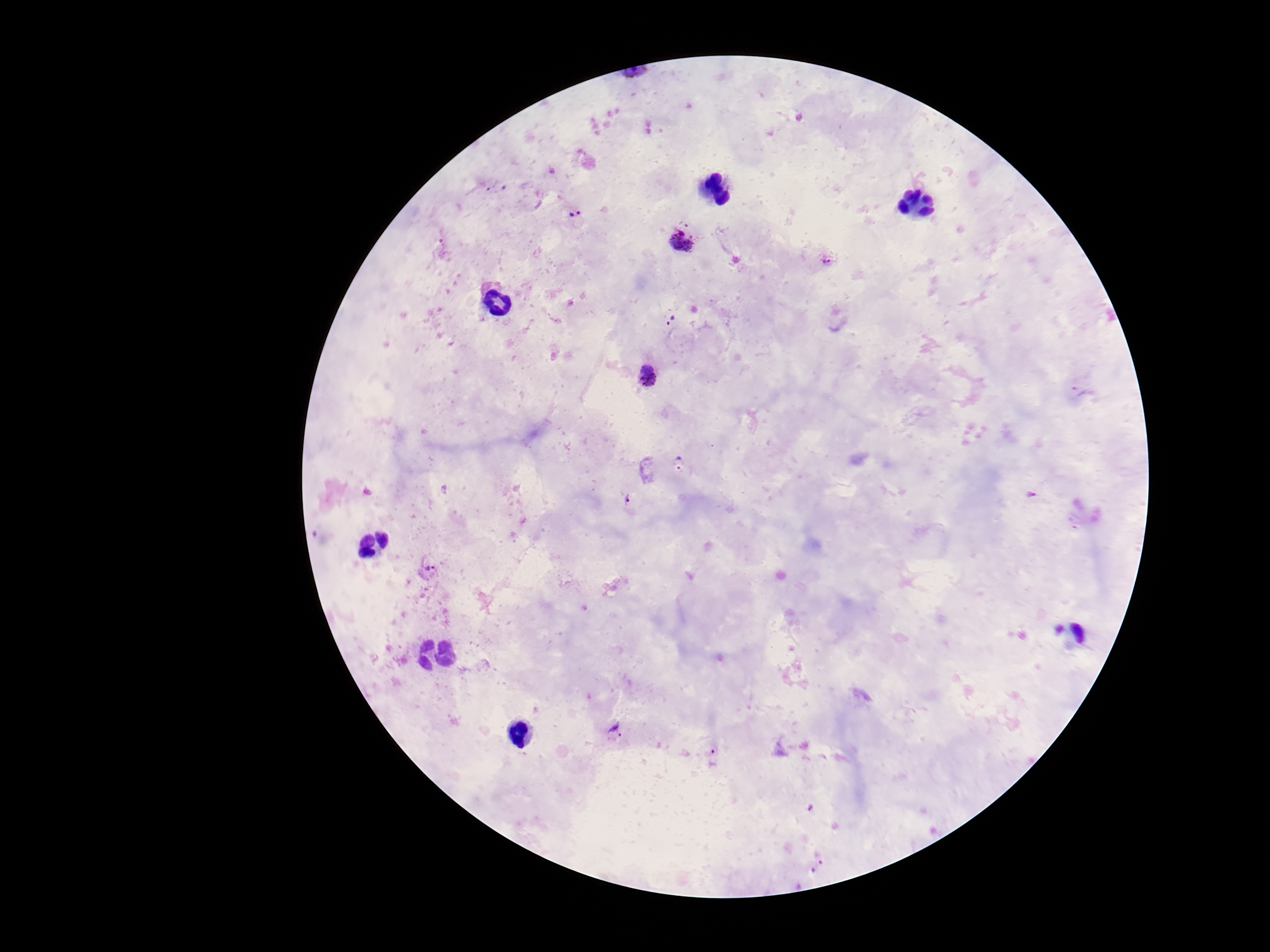

Plasmodium parasite locations = approximate centers as (x, y) in pixels: (497, 188), (575, 212), (681, 239), (827, 259), (672, 318), (649, 375), (1084, 392), (678, 463), (1030, 496), (629, 501), (431, 568), (615, 729), (713, 756), (818, 867)
preparation = thick blood film
magnification = 100x
capture = smartphone camera through the microscope eyepiece
image size = 1270×952 pixels
field of view = one from this slide
stain = Giemsa
patient malaria status = infected